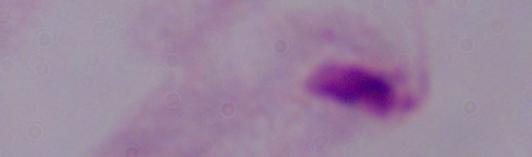

magnification = 1000x
modality = photomicrograph
identification = trichomonad